Assess the morphology of the erythrocytes.
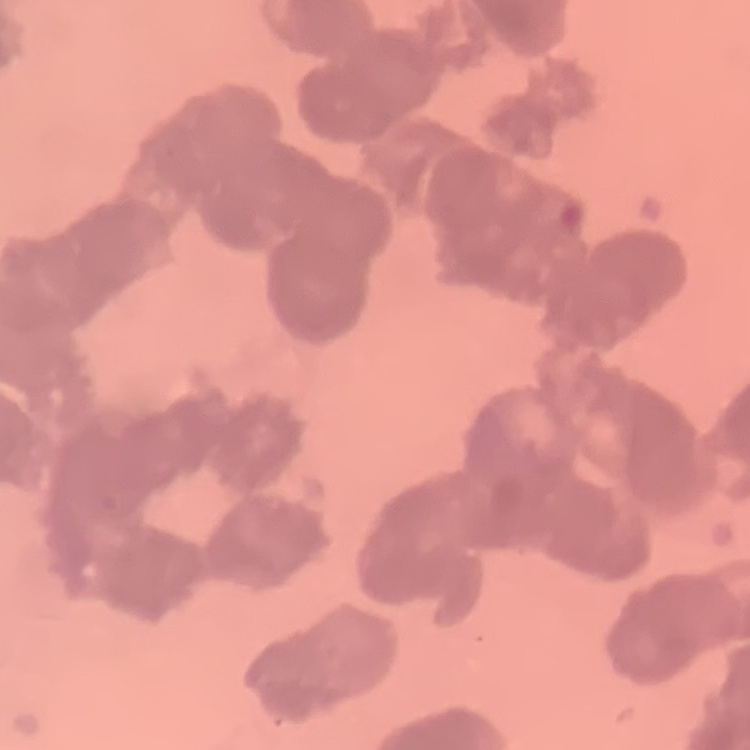
Rouleaux formation.

One tile cut from a larger photomicrograph. Field's or Giemsa stain. Thin blood film.